Classify this cell by malaria status.
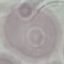

It is uninfected.

Summary:
  - Stain: Giemsa
  - Capture: smartphone camera at the microscope eyepiece
  - Image type: cell patch, automatically extracted from a larger field of view and resized to 64 × 64 pixels
  - Preparation: thin smear